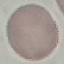

malaria status = uninfected
preparation = thin smear
capture = smartphone camera at the microscope eyepiece
image type = automatically extracted cell patch, resized to 64 × 64 pixels
stain = Giemsa